Report the malaria status of this cell.
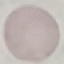

Uninfected.

Summary:
  - Image type: automatically extracted cell patch, resized to 64 × 64 pixels
  - Stain: Giemsa
  - Capture: smartphone through the microscope eyepiece
  - Preparation: thin smear